Point out each Plasmodium parasite.
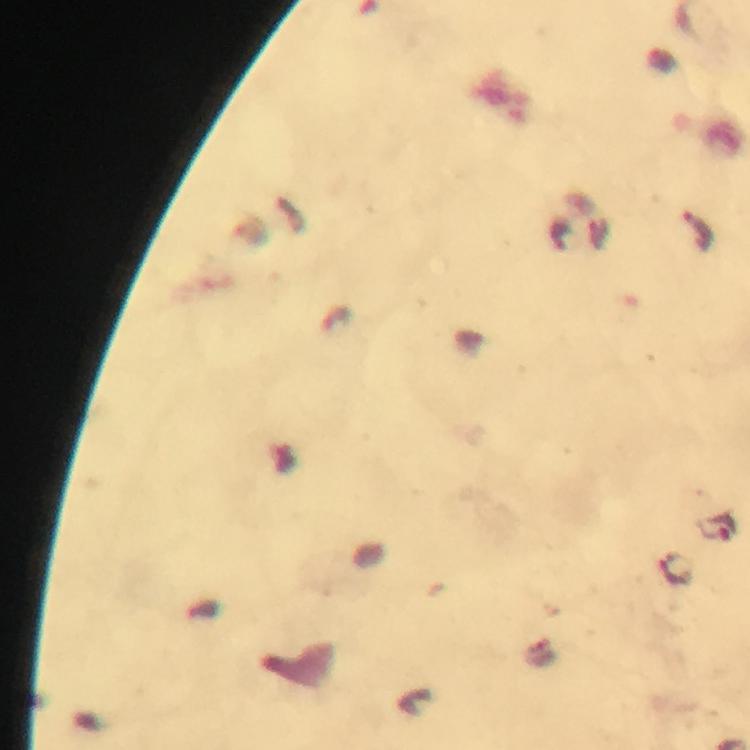

Approximate object centers, in pixels from the top-left corner.
Plasmodium parasites: (x=700, y=230), (x=719, y=528), (x=673, y=566).

stain = Giemsa
preparation = thick smear
immersion oil = used
cropped from = a single field of view
image size = 750×750 pixels
magnification = 100x
context = from a diagnostic examination for malaria
capture = smartphone camera through the microscope